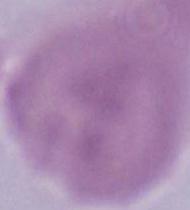

modality = micrograph
magnification = 1000x
identification = erythrocyte